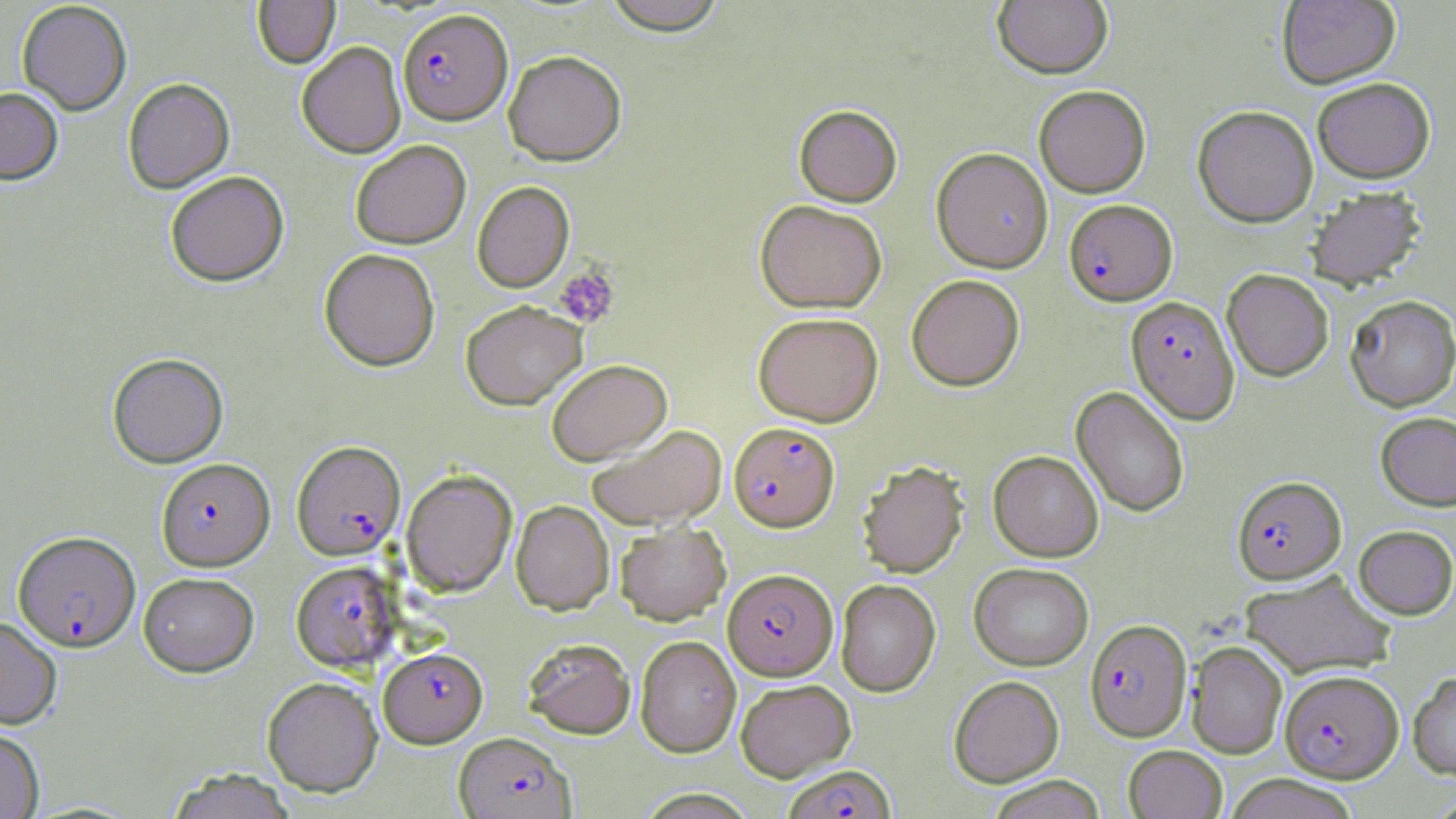 Approximate bounding boxes as (x1,y1)-(x2,y2) corner pairs in pixels. Uninfected red blood cell locations: (600,0)-(730,36), (1277,0)-(1400,88), (17,1)-(132,115), (252,1)-(340,69), (992,1)-(1112,78), (297,42)-(406,158), (504,51)-(626,166), (1312,77)-(1435,182), (123,78)-(234,193), (1034,85)-(1151,197), (0,87)-(63,185), (793,105)-(902,206), (1193,105)-(1318,227), (350,140)-(471,249), (931,147)-(1053,273), (165,171)-(289,287), (472,181)-(574,292), (1305,186)-(1426,289), (754,200)-(887,313), (319,248)-(440,371), (1222,268)-(1334,381), (906,274)-(1024,391), (1345,294)-(1456,411), (460,300)-(587,410), (753,312)-(883,427), (107,352)-(228,468), (546,359)-(672,465), (1072,386)-(1189,518), (1376,411)-(1456,511), (587,424)-(727,529), (989,450)-(1103,561), (858,460)-(968,578), (401,469)-(517,597), (511,500)-(614,615), (615,522)-(731,624), (1353,525)-(1456,619), (969,562)-(1094,670), (1240,571)-(1397,678), (138,572)-(259,676), (835,579)-(941,697), (0,615)-(62,728), (635,635)-(741,757), (522,638)-(636,739), (1186,640)-(1287,758), (1408,671)-(1456,778), (949,675)-(1064,787), (262,676)-(382,796), (735,678)-(856,781), (0,727)-(45,818), (1123,744)-(1227,819), (165,768)-(297,819), (1222,774)-(1361,819), (985,775)-(1107,819), (631,788)-(761,818). Platelet locations: (555,265)-(620,328). Plasmodium falciparum-infected red blood cell locations: (398,8)-(512,124), (1064,199)-(1177,305), (1126,296)-(1239,424), (729,422)-(839,531), (291,440)-(406,560), (156,458)-(275,570), (1232,476)-(1346,583), (12,533)-(139,654), (291,561)-(400,672), (723,571)-(837,683), (1085,619)-(1191,741), (379,647)-(487,747), (1280,669)-(1403,782), (453,732)-(575,819), (782,765)-(896,819). Slide-level diagnosis: Plasmodium falciparum. Light microscopy. Thin blood smear. May-Grünwald-Giemsa stain. Image is 1456×819 pixels. One field of a larger specimen. Captured at 1000x magnification.